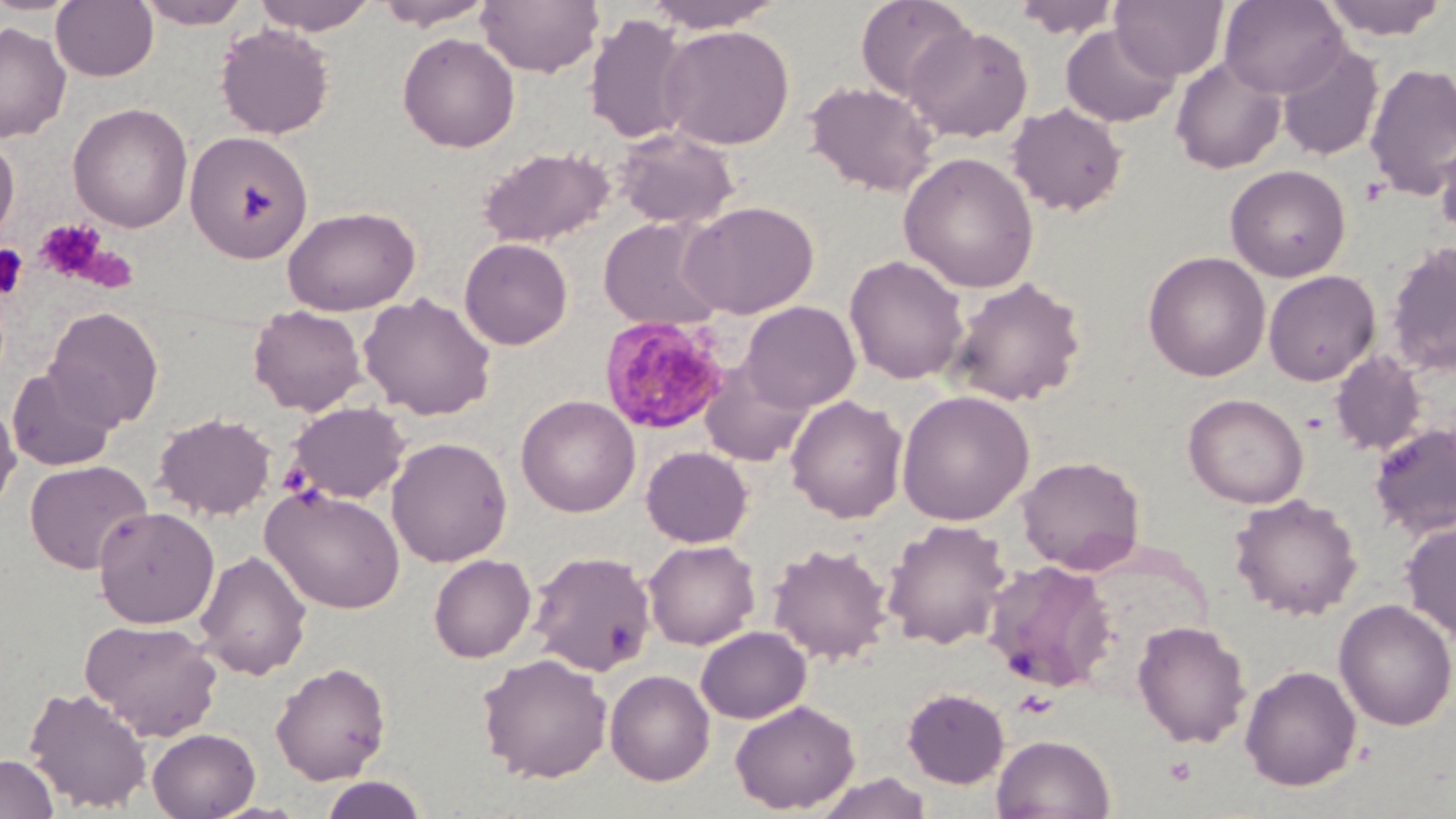
{
  "slide_level_diagnosis": "Plasmodium malariae",
  "uninfected_red_blood_cell_locations": "approximate bounding boxes as (x1,y1)-(x2,y2) corner pairs in pixels: (135,0)-(254,29), (252,0)-(378,34), (375,0)-(496,30), (477,0)-(604,77), (641,0)-(789,32), (855,0)-(975,102), (1013,0)-(1121,40), (1110,0)-(1228,81), (1219,0)-(1348,97), (1319,0)-(1449,40), (51,1)-(159,82), (584,13)-(695,143), (0,22)-(71,143), (216,24)-(335,139), (659,24)-(795,150), (906,24)-(1033,142), (1061,25)-(1179,128), (398,32)-(520,153), (1276,42)-(1384,161), (1170,55)-(1287,174), (1364,62)-(1456,201), (805,81)-(938,197), (68,102)-(193,232), (1007,103)-(1129,216), (613,128)-(740,229), (184,131)-(314,263), (1435,131)-(1456,242), (0,134)-(19,246), (476,146)-(615,249), (898,152)-(1040,293), (1225,164)-(1351,282), (679,200)-(819,319), (282,205)-(421,316), (598,217)-(726,332), (459,238)-(573,349), (1385,241)-(1456,376), (1143,250)-(1271,381), (844,255)-(968,384), (1263,270)-(1380,386), (948,277)-(1086,406), (359,292)-(497,420), (739,301)-(861,413), (248,305)-(367,416), (44,307)-(164,430), (1329,351)-(1426,455), (701,363)-(812,468), (6,367)-(119,471), (12,370)-(133,572), (896,390)-(1035,526), (1183,393)-(1309,508), (786,394)-(908,523), (516,395)-(640,517), (0,397)-(21,517), (286,401)-(410,504), (153,411)-(277,520), (1368,422)-(1456,539), (386,437)-(513,567), (641,446)-(753,547), (1017,455)-(1146,575), (25,460)-(152,574), (261,485)-(406,614), (1229,493)-(1363,620), (93,506)-(219,629), (882,519)-(1012,650), (1401,521)-(1456,642), (643,539)-(760,650), (767,542)-(893,664), (195,549)-(311,680), (528,550)-(657,676), (429,554)-(536,662), (982,560)-(1118,692), (1334,599)-(1456,731), (80,618)-(223,741), (1132,620)-(1252,748), (694,625)-(811,724), (477,652)-(613,783), (270,661)-(392,785), (1240,664)-(1362,791), (604,669)-(715,786), (24,686)-(153,812), (902,687)-(1009,788), (730,699)-(860,814), (147,727)-(261,818), (992,733)-(1115,818), (0,754)-(59,818), (816,772)-(933,819), (318,775)-(427,818)",
  "field_of_view": "single",
  "modality": "light microscopy",
  "platelet_locations": "approximate bounding boxes as (x1,y1)-(x2,y2) corner pairs in pixels: (34,218)-(110,284), (0,244)-(28,300), (1164,757)-(1196,785)",
  "stain": "May-Grünwald-Giemsa",
  "image_size": "1456×819 pixels",
  "plasmodium_malariae_infected_red_blood_cell_locations": "approximate bounding boxes as (x1,y1)-(x2,y2) corner pairs in pixels: (599,316)-(731,436)",
  "preparation": "thin blood film",
  "magnification": "1000x"
}